Give the extent of all Plasmodium falciparum-infected red blood cells.
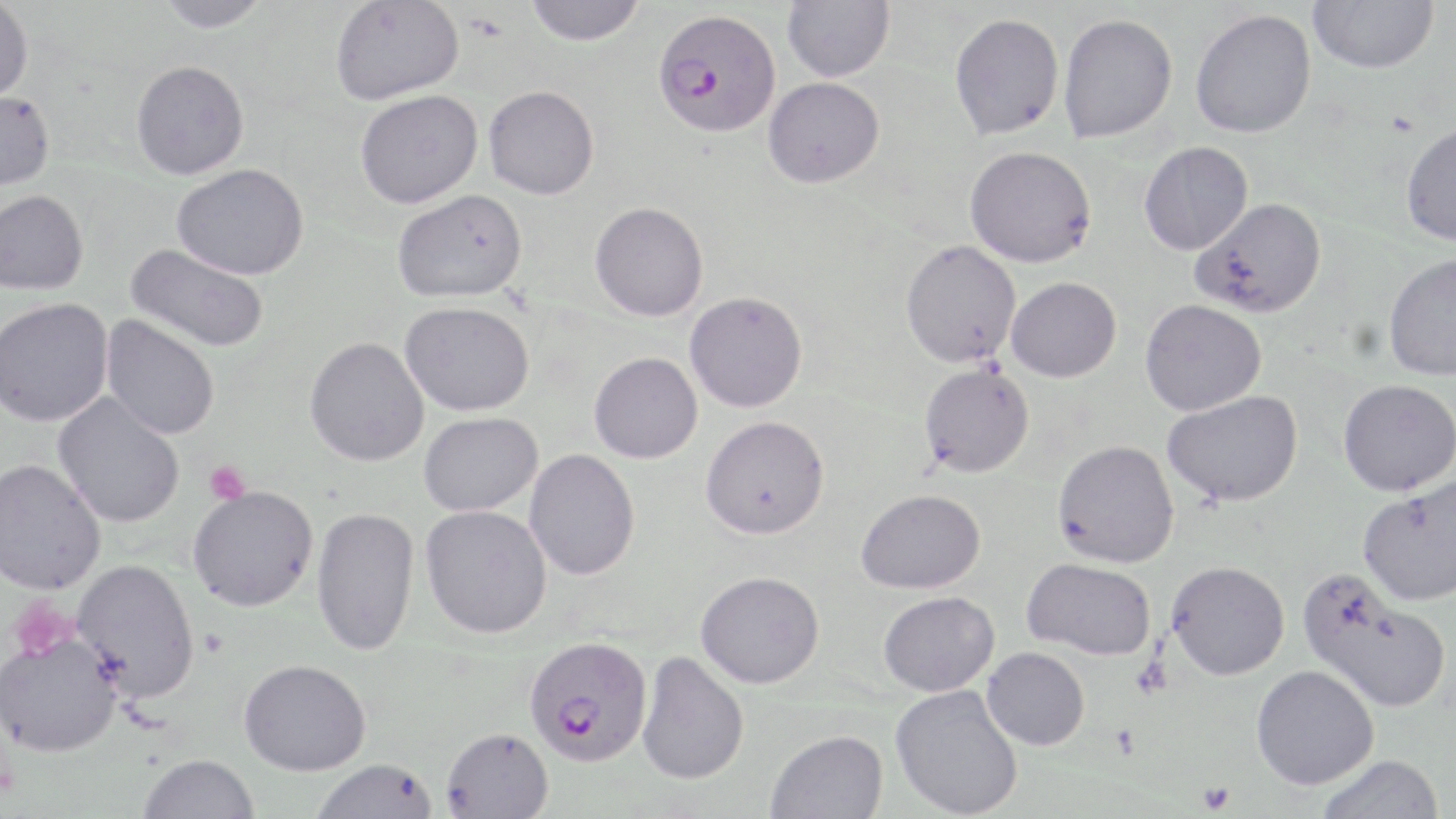

Approximate bounding boxes as (x1, y1, x2, y2) in pixels.
Plasmodium falciparum-infected red blood cells: (652, 10, 781, 139), (524, 635, 653, 766).

Summary:
  - Uninfected red blood cell locations: (156, 0, 271, 35), (330, 0, 464, 107), (782, 0, 895, 82), (1308, 0, 1439, 73), (0, 1, 33, 106), (524, 1, 646, 47), (1190, 8, 1316, 138), (1058, 13, 1177, 142), (949, 14, 1064, 139), (130, 64, 250, 183), (763, 77, 884, 188), (483, 87, 600, 201), (355, 92, 483, 211), (0, 93, 55, 192), (1400, 122, 1456, 246), (1139, 141, 1253, 255), (965, 145, 1096, 267), (171, 165, 309, 282), (393, 191, 528, 305), (0, 192, 88, 297), (1190, 197, 1327, 318), (589, 202, 709, 322), (900, 239, 1021, 367), (124, 243, 269, 353), (1383, 252, 1456, 381), (1006, 276, 1122, 382), (685, 291, 807, 412), (1140, 298, 1266, 416), (0, 299, 114, 429), (399, 302, 534, 417), (100, 315, 219, 441), (304, 338, 429, 468), (589, 352, 702, 463), (919, 363, 1035, 478), (1338, 379, 1456, 496), (1163, 390, 1303, 507), (52, 392, 185, 529), (419, 412, 543, 517), (700, 415, 829, 539), (1052, 439, 1180, 568), (524, 449, 640, 580), (0, 460, 106, 597), (1358, 478, 1456, 606), (188, 487, 317, 612), (857, 489, 986, 594), (420, 504, 552, 638), (311, 506, 420, 657), (1022, 557, 1157, 660), (73, 559, 200, 704), (1166, 560, 1290, 680), (696, 570, 824, 688), (1297, 570, 1452, 713), (878, 591, 999, 696), (0, 635, 123, 760), (981, 647, 1090, 750), (637, 651, 750, 786), (239, 659, 371, 776), (1251, 664, 1379, 790), (891, 685, 1024, 818), (441, 726, 554, 818), (765, 729, 890, 819), (1315, 753, 1444, 819), (138, 755, 260, 819), (310, 758, 439, 818)
  - Platelet locations: (204, 460, 251, 504), (8, 596, 79, 660), (1198, 779, 1235, 814)
  - Slide-level diagnosis: Plasmodium falciparum
  - Stain: May-Grünwald-Giemsa
  - Modality: light microscopy
  - Preparation: thin blood film
  - Image size: 1456×819 pixels
  - Field of view: one of a larger specimen
  - Magnification: 1000x